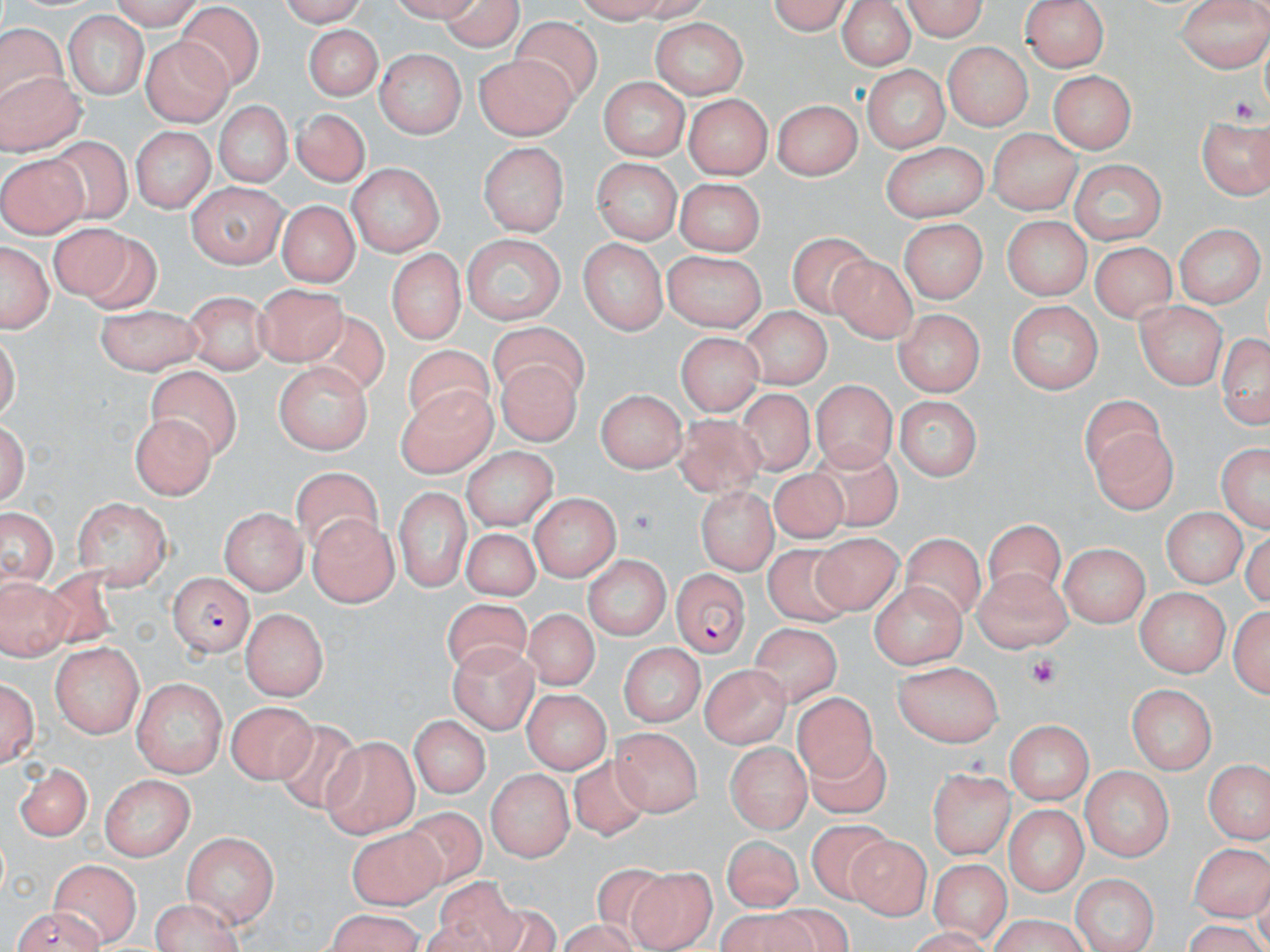

Summary:
  - Coordinate format: approximate bounding boxes as (x1,y1)-(x2,y2) corner pairs in pixels
  - Uninfected red blood cell locations: (98,0)-(204,27), (270,0)-(374,24), (436,0)-(524,55), (576,0)-(715,25), (768,0)-(858,34), (901,0)-(990,40), (1178,0)-(1270,71), (832,1)-(917,72), (1024,2)-(1107,74), (181,5)-(267,87), (63,14)-(147,100), (510,17)-(601,109), (651,18)-(749,100), (1,21)-(63,110), (301,24)-(384,101), (138,33)-(231,125), (943,43)-(1030,130), (374,50)-(466,136), (476,55)-(578,138), (0,62)-(84,152), (865,65)-(948,153), (1049,70)-(1135,156), (598,77)-(687,162), (684,96)-(770,179), (774,96)-(859,180), (212,102)-(296,189), (297,112)-(368,185), (1197,112)-(1269,200), (990,127)-(1080,215), (133,128)-(212,212), (51,134)-(138,225), (481,142)-(570,234), (884,144)-(989,223), (0,151)-(84,238), (590,159)-(682,247), (1067,161)-(1165,245), (348,165)-(446,257), (678,176)-(765,253), (188,183)-(287,267), (274,201)-(359,289), (999,218)-(1093,300), (896,219)-(987,303), (47,222)-(131,306), (1176,223)-(1260,309), (84,233)-(160,316), (460,234)-(565,327), (787,236)-(882,321), (1,238)-(51,332), (578,239)-(666,333), (1088,245)-(1178,328), (390,252)-(463,344), (657,252)-(766,332), (832,256)-(915,341), (257,285)-(348,365), (184,291)-(268,372), (1007,302)-(1100,394), (1136,302)-(1226,390), (95,306)-(204,374), (300,307)-(389,404), (742,307)-(830,386), (892,311)-(984,393), (494,321)-(589,401), (1217,326)-(1270,430), (675,332)-(763,414), (403,344)-(493,433), (495,359)-(579,447), (275,363)-(371,456), (143,365)-(241,464), (813,379)-(897,472), (391,386)-(502,484), (739,387)-(815,480), (593,390)-(688,471), (1082,395)-(1171,481), (892,397)-(980,483), (124,411)-(214,494), (670,415)-(767,505), (1092,425)-(1179,513), (803,440)-(907,534), (1216,441)-(1270,535), (464,447)-(555,532), (767,466)-(852,548), (289,470)-(389,561), (694,486)-(774,574), (395,488)-(473,589), (527,495)-(621,581), (73,496)-(172,591), (2,503)-(57,588), (220,506)-(305,595), (1161,508)-(1244,588), (984,514)-(1061,601), (306,515)-(398,605), (455,526)-(547,607), (806,532)-(903,613), (905,534)-(985,627), (1061,540)-(1149,630), (761,546)-(863,630), (583,556)-(671,641), (969,567)-(1070,649), (1,570)-(80,667), (869,581)-(971,666), (1137,589)-(1227,676), (441,596)-(533,682), (1231,605)-(1268,700), (241,608)-(329,701), (522,613)-(605,695), (753,622)-(840,700), (616,641)-(703,727), (50,643)-(147,739), (450,644)-(534,732), (894,661)-(1001,747), (703,666)-(790,744), (1,674)-(41,771), (134,677)-(227,777), (1129,683)-(1215,773), (520,686)-(614,770), (792,693)-(882,787), (227,701)-(318,784), (411,711)-(493,796), (1005,721)-(1094,802), (267,724)-(367,816), (607,730)-(715,819), (321,736)-(417,836), (726,738)-(811,835), (806,739)-(890,819), (559,757)-(649,846), (1207,758)-(1268,844), (17,760)-(94,839), (930,765)-(1014,859), (485,767)-(575,860), (1079,769)-(1173,861), (98,774)-(194,859), (397,804)-(498,891), (1006,805)-(1085,897), (802,819)-(895,905), (349,828)-(446,908), (183,831)-(277,927), (724,835)-(805,910), (845,837)-(935,916), (1193,842)-(1269,919), (927,859)-(1016,947), (52,860)-(141,943), (592,864)-(671,948), (631,866)-(718,948), (1073,873)-(1156,952), (426,879)-(531,952), (147,898)-(248,952), (11,907)-(105,952), (720,907)-(822,952), (320,910)-(428,952), (983,919)-(1091,951)
  - Platelet locations: (1027,655)-(1059,688)
  - Plasmodium falciparum-infected red blood cell locations: (675,570)-(748,661), (169,573)-(251,657)
  - Slide-level diagnosis: Plasmodium falciparum
  - Stain: May-Grünwald-Giemsa
  - Preparation: thin blood film
  - Modality: light microscopy
  - Magnification: 1000x
  - Field of view: one of a larger specimen
  - Image size: 1270×952 pixels